Assess the morphology of the red blood cells.
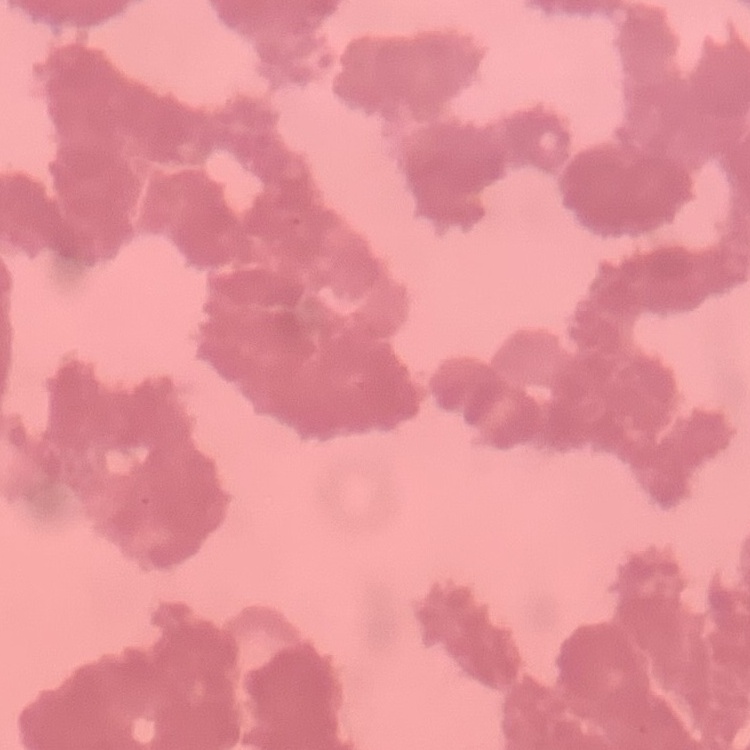
Rouleaux formation.

{
  "image_type": "one tile cut from a larger photomicrograph",
  "preparation": "thin blood film",
  "stain": "Field's or Giemsa"
}